Report the malaria status of this cell.
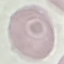
It is uninfected.

Giemsa-stained preparation. Automatically extracted cell patch, resized to 64 × 64 pixels. Photographed with a smartphone camera at the microscope eyepiece. Thin blood smear.